State which parasite is depicted.
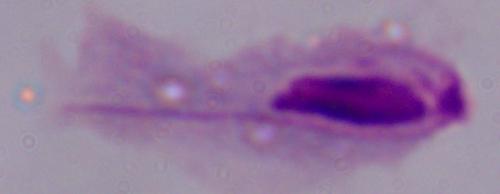

This is a trichomonad.

Photomicrograph. Captured at 1000x magnification.